Classify this cell by malaria status.
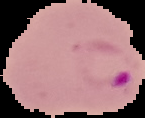

It is parasitized.

From a thin blood smear. The area outside the segmented cell region is set to black. Image is 145×118 pixels.